Identify the parasite.
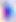
Toxoplasma gondii.

Summary:
  - Magnification: 400x
  - Modality: photomicrograph